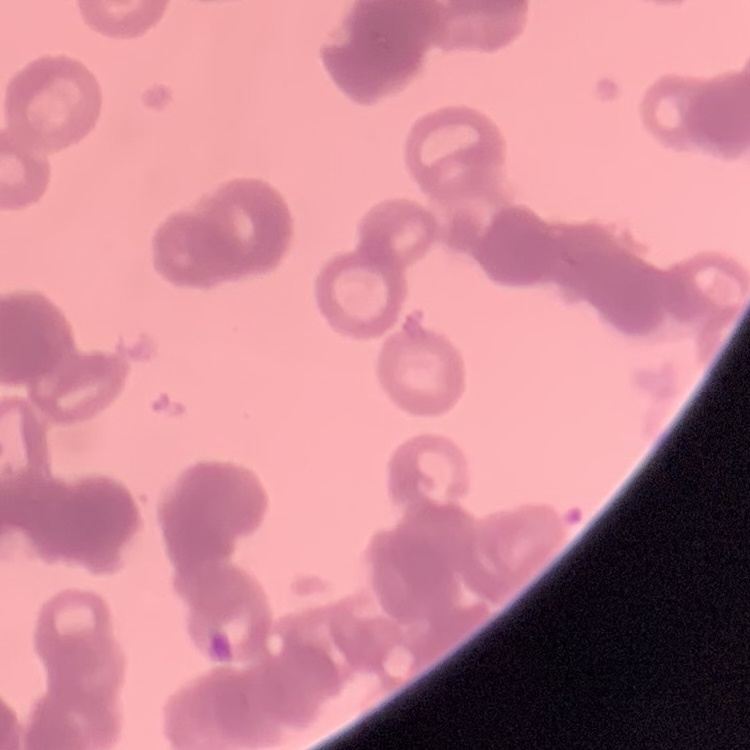
erythrocyte_morphology: rouleaux formation
stain: Field's or Giemsa
preparation: thin blood smear
image_type: square crop of a larger photomicrograph